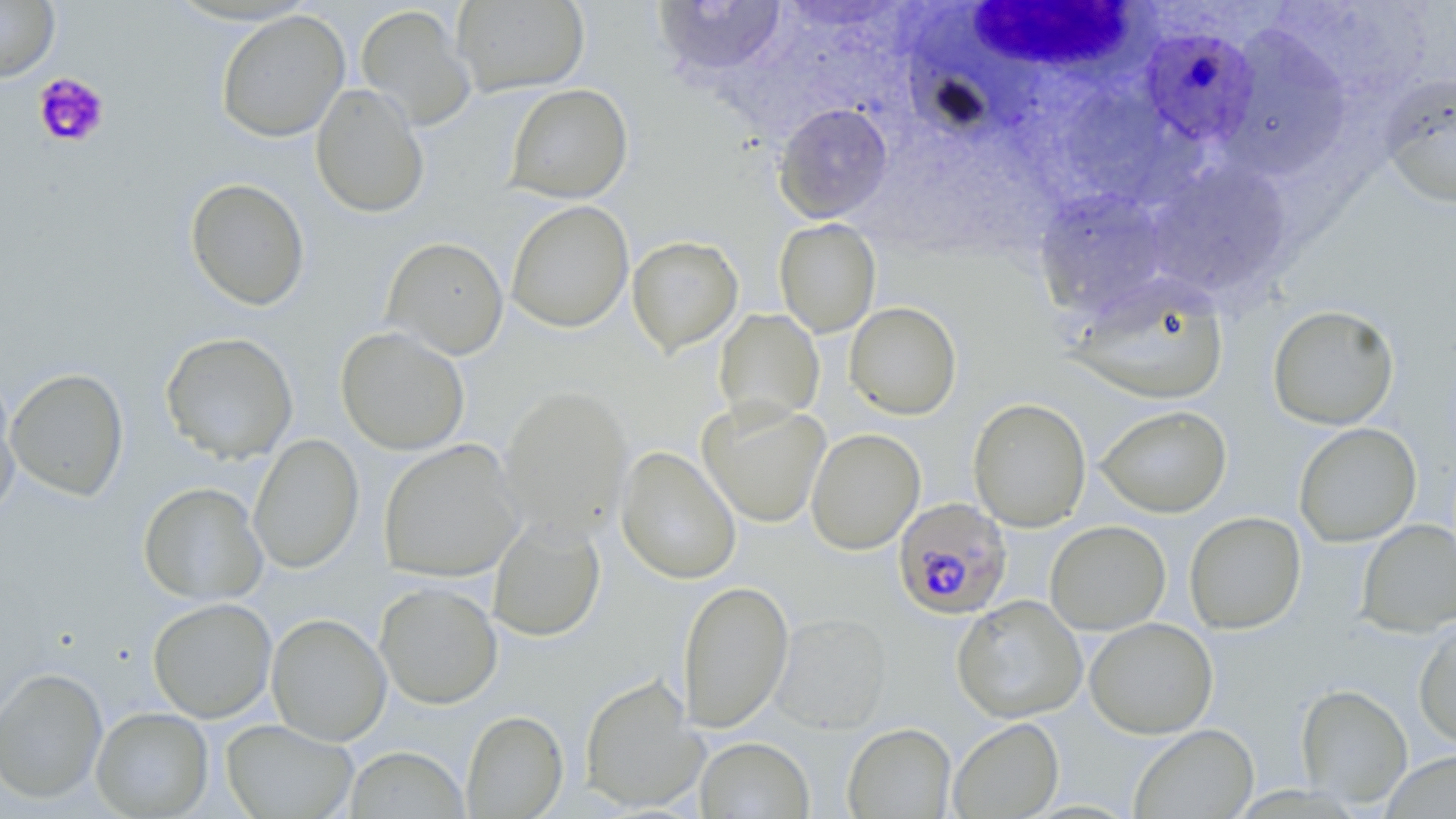 Approximate bounding boxes as (x1, y1, x2, y2) in pixels. White blood cell locations: (960, 1, 1152, 89). Plasmodium falciparum-infected red blood cell locations: (1137, 28, 1258, 151), (890, 498, 1010, 620). Platelet locations: (33, 73, 110, 148). Uninfected red blood cell locations: (0, 0, 60, 83), (451, 0, 590, 96), (652, 1, 789, 80), (355, 4, 477, 131), (215, 9, 350, 142), (1219, 25, 1352, 176), (1379, 72, 1456, 208), (310, 83, 429, 219), (505, 83, 633, 204), (1062, 89, 1176, 205), (773, 102, 893, 223), (1146, 161, 1295, 300), (185, 177, 310, 311), (1034, 189, 1172, 317), (506, 200, 634, 333), (774, 219, 881, 338), (627, 236, 743, 356), (382, 237, 509, 360), (1067, 274, 1229, 405), (844, 302, 962, 420), (1267, 304, 1400, 431), (714, 308, 824, 426), (335, 326, 470, 455), (160, 331, 299, 464), (5, 367, 129, 501), (0, 376, 21, 521), (499, 386, 632, 539), (968, 397, 1092, 532), (697, 398, 832, 528), (1095, 405, 1232, 518), (1294, 422, 1421, 547), (806, 428, 925, 555), (248, 434, 364, 574), (378, 439, 525, 582), (615, 445, 741, 585), (138, 482, 268, 606), (1184, 511, 1307, 634), (488, 517, 605, 641), (1356, 519, 1456, 637), (1045, 520, 1171, 635), (677, 579, 794, 733), (374, 582, 503, 710), (952, 594, 1087, 723), (147, 597, 277, 722), (770, 612, 892, 734), (266, 613, 392, 746), (1084, 617, 1218, 739), (1413, 619, 1456, 747), (0, 667, 108, 804), (579, 673, 708, 812), (1296, 684, 1412, 807), (91, 706, 214, 818), (461, 710, 568, 818), (948, 717, 1064, 818), (221, 719, 358, 818), (842, 722, 956, 818), (1129, 724, 1259, 818), (696, 736, 814, 818), (344, 746, 470, 818), (1381, 750, 1456, 819). Slide-level diagnosis: Plasmodium falciparum. May-Grünwald-Giemsa stain. Light microscopy. Image is 1456×819 pixels. Captured at 1000x magnification. Single field of view. Thin blood smear.